Identify the blood parasite species.
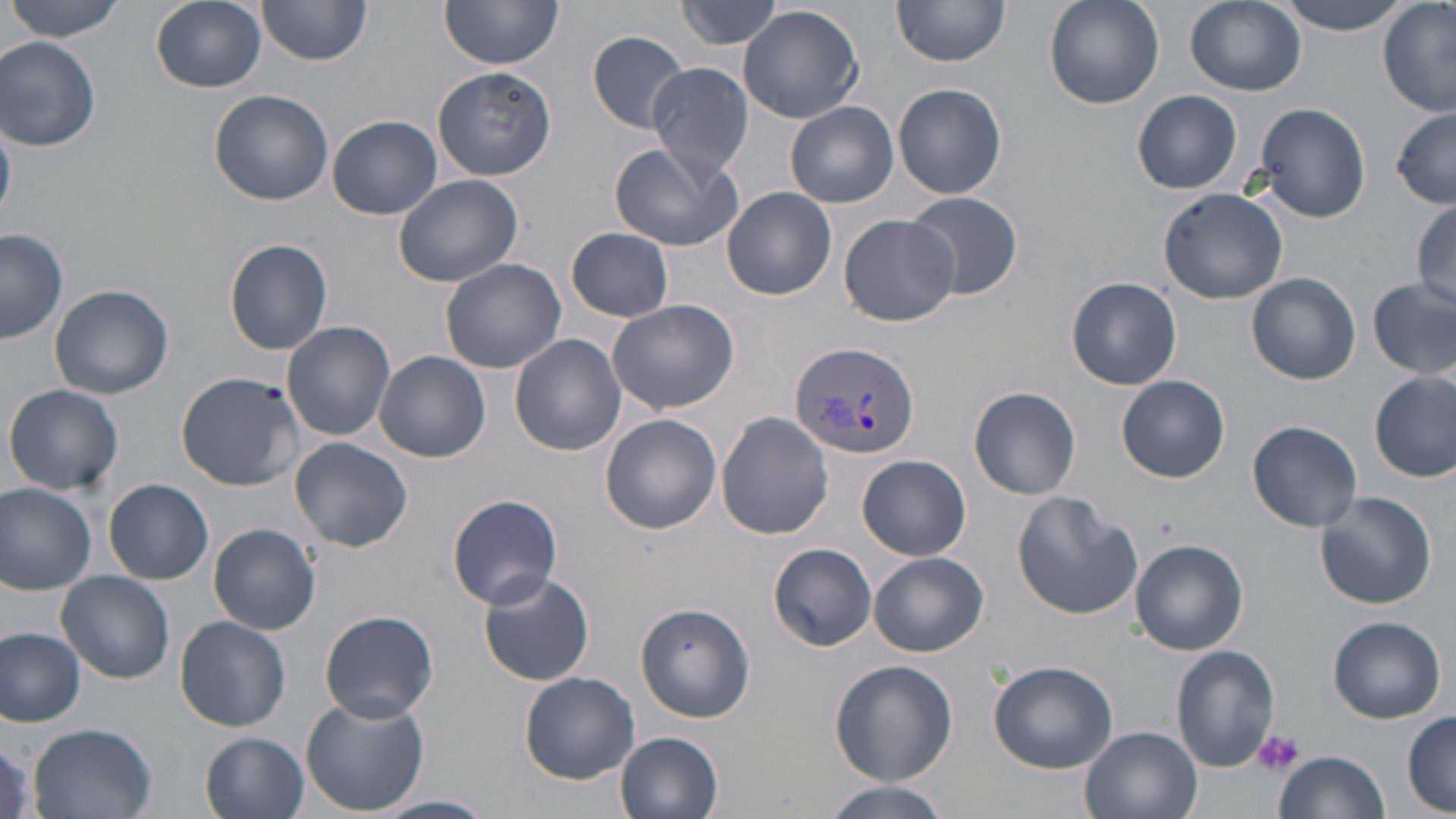
Plasmodium vivax.

Approximate bounding boxes as (x1,y1)-(x2,y2) corner pairs in pixels. Uninfected red blood cell locations: (7,0)-(128,42), (150,0)-(266,92), (258,0)-(372,66), (440,0)-(563,70), (675,0)-(788,50), (893,0)-(1013,68), (1043,0)-(1163,109), (1185,0)-(1305,96), (1270,0)-(1414,33), (1379,2)-(1456,116), (738,5)-(864,124), (588,32)-(692,133), (0,37)-(102,151), (645,60)-(755,178), (433,68)-(556,182), (894,83)-(1007,200), (210,90)-(332,206), (1132,90)-(1242,194), (786,101)-(898,208), (1254,102)-(1370,223), (1392,109)-(1456,208), (328,115)-(442,220), (610,142)-(740,254), (574,162)-(705,306), (394,174)-(523,286), (722,187)-(836,300), (1159,188)-(1287,304), (905,191)-(1023,301), (1410,195)-(1455,313), (839,213)-(959,327), (567,227)-(674,322), (0,230)-(68,343), (225,239)-(334,355), (438,257)-(567,373), (1247,272)-(1361,384), (1066,277)-(1182,390), (1369,277)-(1456,382), (49,284)-(174,399), (608,299)-(739,416), (282,321)-(396,440), (510,334)-(625,456), (374,351)-(489,462), (1371,370)-(1455,483), (176,372)-(305,490), (1118,375)-(1229,483), (4,383)-(124,497), (969,384)-(1081,499), (716,411)-(834,538), (600,413)-(721,534), (1247,420)-(1363,531), (292,436)-(412,551), (858,455)-(971,561), (104,479)-(212,583), (0,483)-(96,595), (1315,490)-(1438,609), (1012,491)-(1142,619), (447,494)-(563,609), (208,522)-(321,634), (1132,539)-(1249,655), (770,543)-(876,651), (870,552)-(988,657), (57,570)-(175,684), (478,571)-(595,687), (635,602)-(756,724), (319,610)-(439,722), (173,615)-(291,732), (1328,616)-(1446,724), (0,628)-(86,726), (1172,646)-(1280,770), (830,660)-(958,786), (989,660)-(1119,772), (521,671)-(639,783), (300,695)-(429,815), (1401,711)-(1456,813), (27,723)-(161,819), (1080,727)-(1201,819), (616,731)-(723,818), (202,733)-(311,819), (1274,750)-(1389,819), (819,779)-(955,819), (375,794)-(497,819). Plasmodium vivax-infected red blood cell locations: (789,340)-(921,462). Platelet locations: (1253,728)-(1305,776). Optical microscopy. Thin blood film. Captured at 1000x magnification. May-Grünwald-Giemsa-stained preparation. Image is 1456×819 pixels. Single field of view.